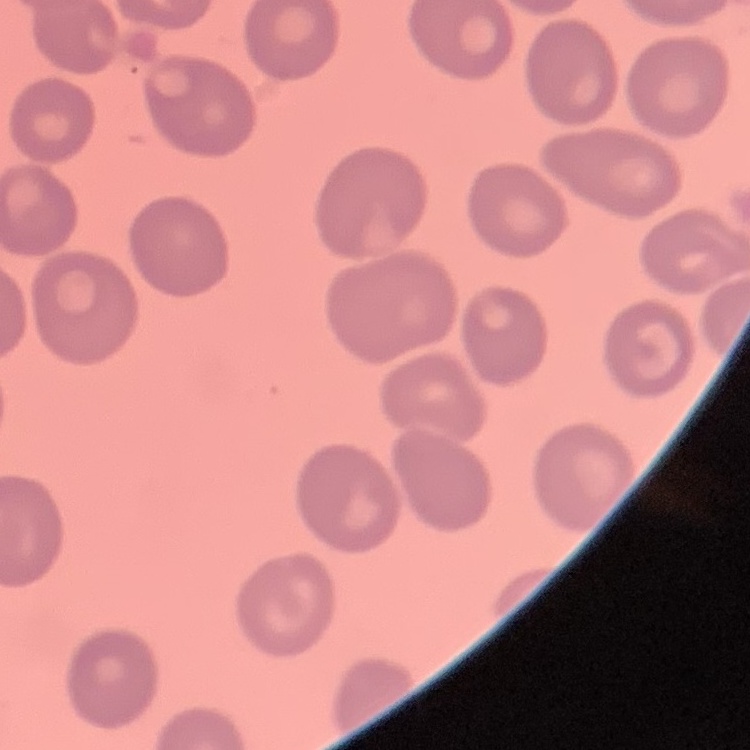
The red blood cells exhibit no rouleaux formation. Square crop of a larger photomicrograph. Field's or Giemsa stain. Thin peripheral smear.